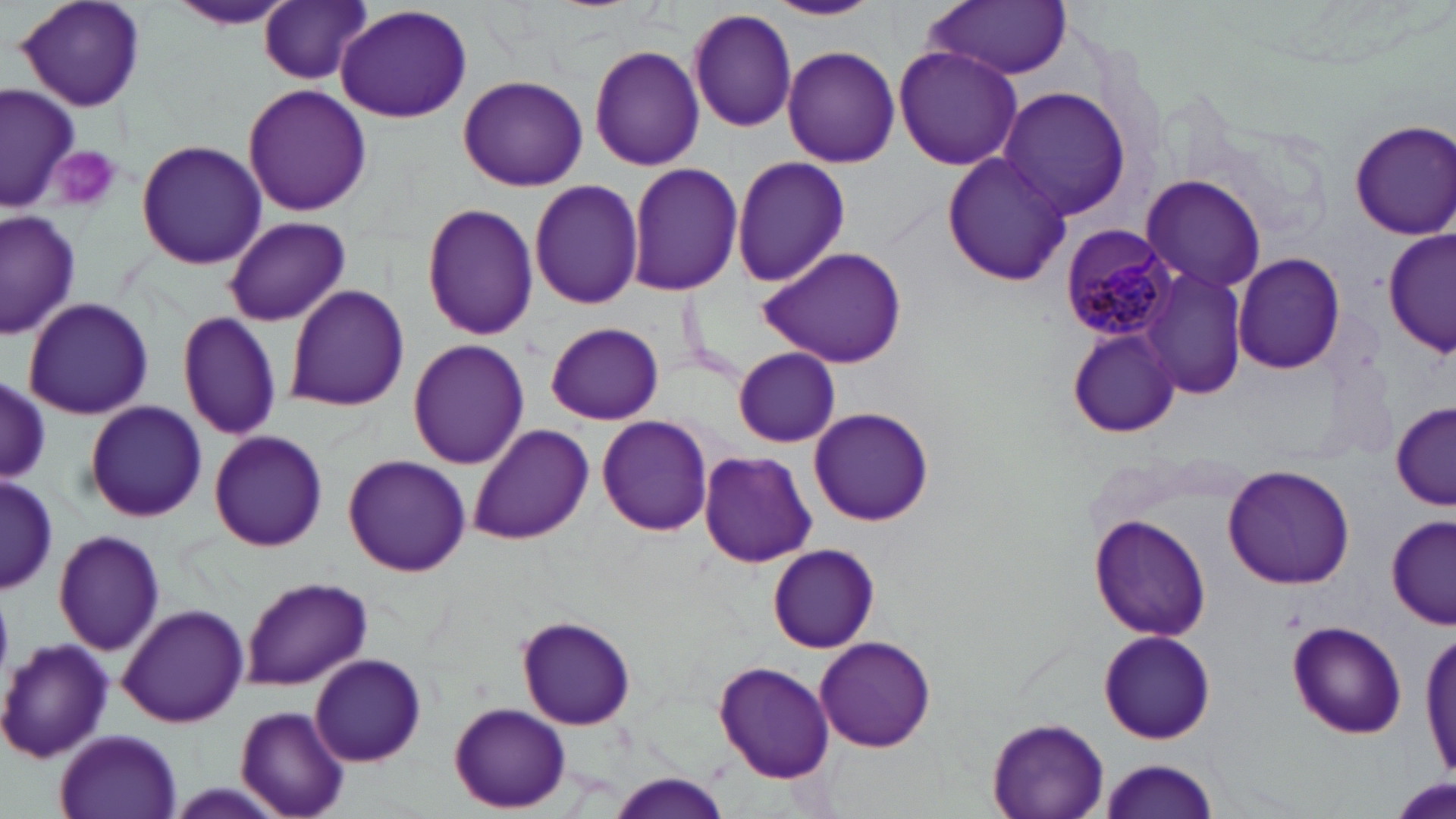

Summary:
  - Coordinate format: approximate bounding boxes as (x1,y1)-(x2,y2) corner pairs in pixels
  - Uninfected red blood cell locations: (763,0)-(885,21), (921,0)-(1074,79), (14,1)-(147,113), (168,1)-(296,31), (260,2)-(372,86), (334,3)-(474,123), (687,8)-(798,133), (585,44)-(706,173), (892,45)-(1023,171), (782,46)-(901,169), (457,74)-(587,192), (2,84)-(78,212), (241,84)-(372,216), (996,87)-(1134,219), (1348,119)-(1456,240), (136,139)-(266,270), (941,153)-(1072,285), (730,156)-(850,288), (626,162)-(743,296), (1139,174)-(1268,295), (529,178)-(646,309), (422,202)-(539,341), (0,208)-(82,339), (223,215)-(351,328), (1383,228)-(1456,357), (756,245)-(910,369), (1232,250)-(1347,375), (1140,264)-(1248,402), (284,283)-(410,414), (22,297)-(153,421), (177,312)-(283,441), (545,322)-(663,425), (1067,323)-(1180,439), (407,340)-(529,469), (733,347)-(841,447), (1,379)-(50,482), (84,399)-(208,522), (1393,399)-(1456,508), (808,406)-(935,526), (597,415)-(715,538), (468,422)-(593,544), (208,430)-(328,551), (697,450)-(817,568), (341,454)-(472,576), (1221,465)-(1356,589), (0,473)-(56,597), (1386,512)-(1454,630), (1089,514)-(1213,643), (52,529)-(165,656), (768,543)-(879,652), (239,575)-(373,689), (116,604)-(250,726), (516,613)-(636,731), (1287,620)-(1407,739), (1098,629)-(1215,746), (1420,630)-(1456,786), (813,636)-(937,753), (2,638)-(115,762), (309,653)-(427,767), (712,661)-(838,784), (450,702)-(571,814), (236,706)-(350,819), (987,717)-(1111,818), (54,729)-(183,819), (1095,755)-(1221,819), (605,772)-(732,817)
  - Plasmodium malariae-infected red blood cell locations: (1061,223)-(1180,341)
  - Platelet locations: (51,145)-(123,213)
  - Slide-level diagnosis: Plasmodium malariae
  - Modality: light microscopy
  - Magnification: 1000x
  - Preparation: thin blood film
  - Image size: 1456×819 pixels
  - Field of view: one of a larger specimen
  - Stain: May-Grünwald-Giemsa